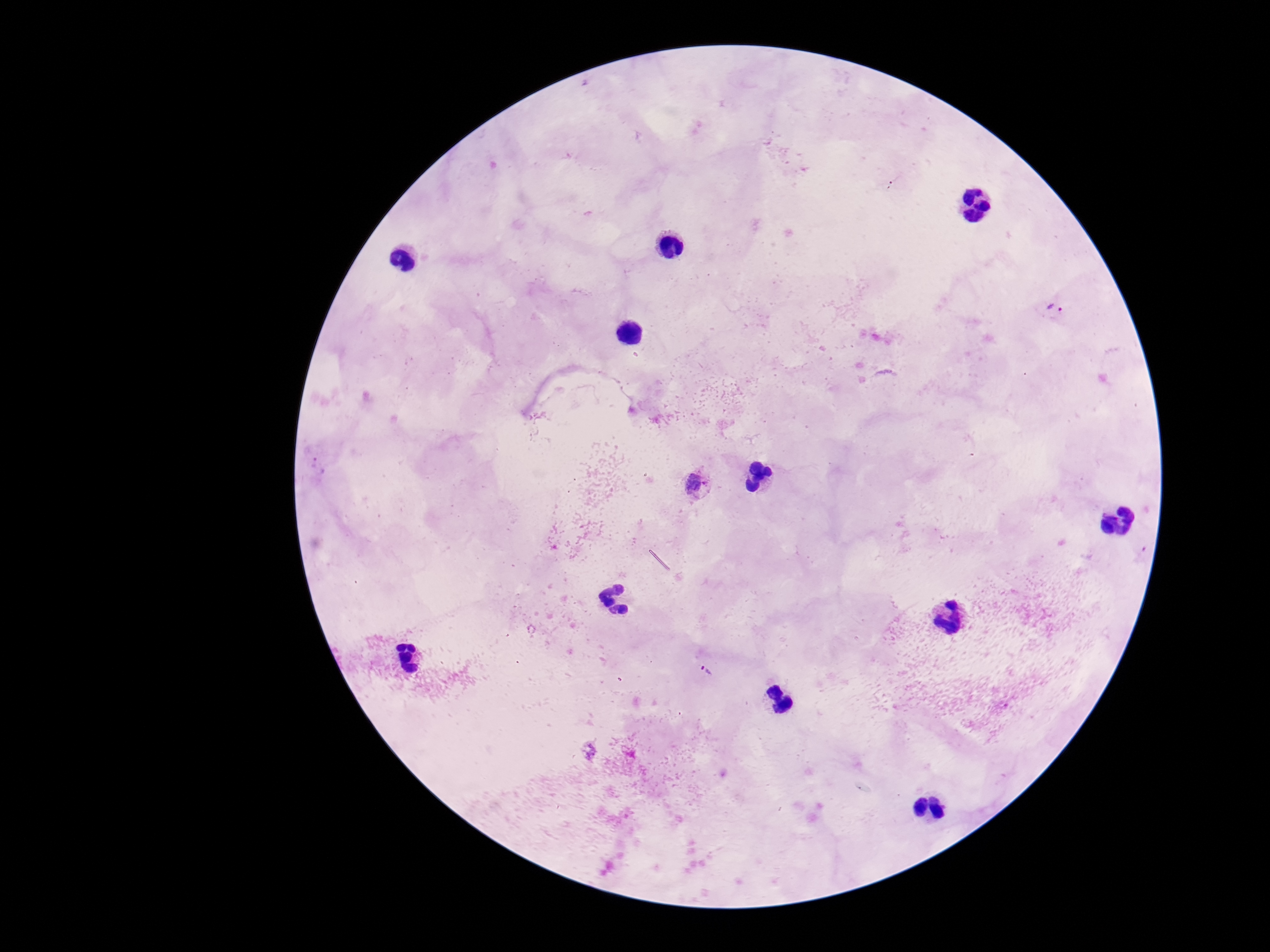

Approximate centers as (x, y) in pixels. Plasmodium parasite locations: (1057, 312), (695, 484), (703, 671). Photographed through the microscope eyepiece with a smartphone camera. 100x magnification. Single field of view. Image is 1270×952 pixels. Giemsa stain. Thick blood film. Patient malaria status: infected.